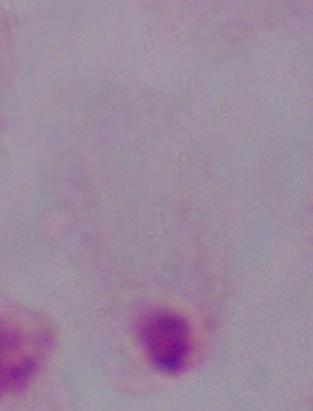

Photomicrograph. A trichomonad is shown. 1000x magnification.